Assess this cell for malaria.
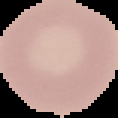
It is uninfected.

preparation: thin blood film
image_type: segmented cell region on a black background
image_size: 118×118 pixels